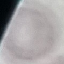
Summary:
  - Result: no malaria parasites detected
  - Preparation: thin smear
  - Capture: smartphone through the microscope eyepiece
  - Image type: automatically extracted cell patch, resized to 64 × 64 pixels
  - Stain: Giemsa